Report the malaria status of this cell.
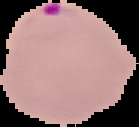
Parasitized.

image size = 139×127 pixels
preparation = thin blood smear
image type = segmented cell region on a black background